Assess the morphology of the erythrocytes.
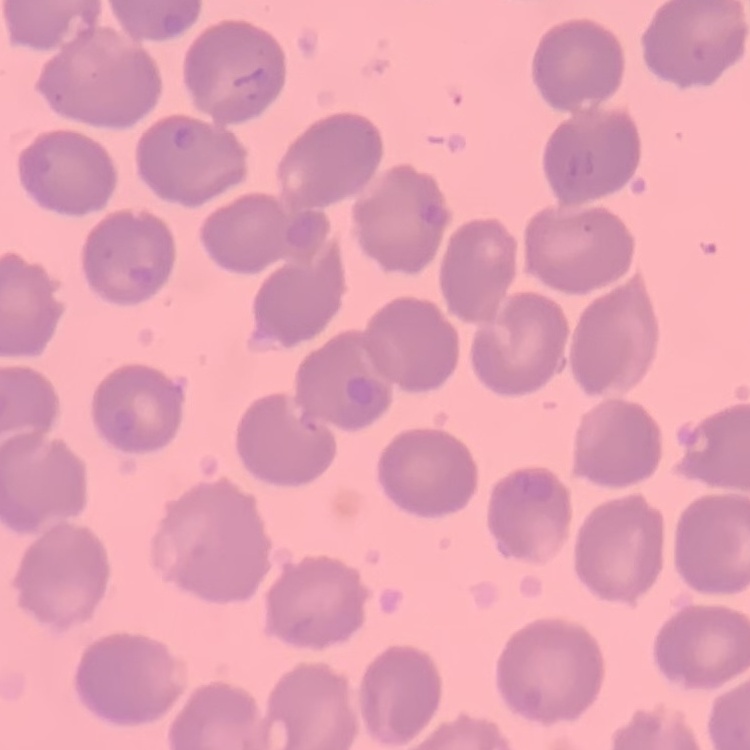
They show no rouleaux formation.

Thin peripheral smear. Field's or Giemsa stain. One tile cut from a larger photomicrograph.